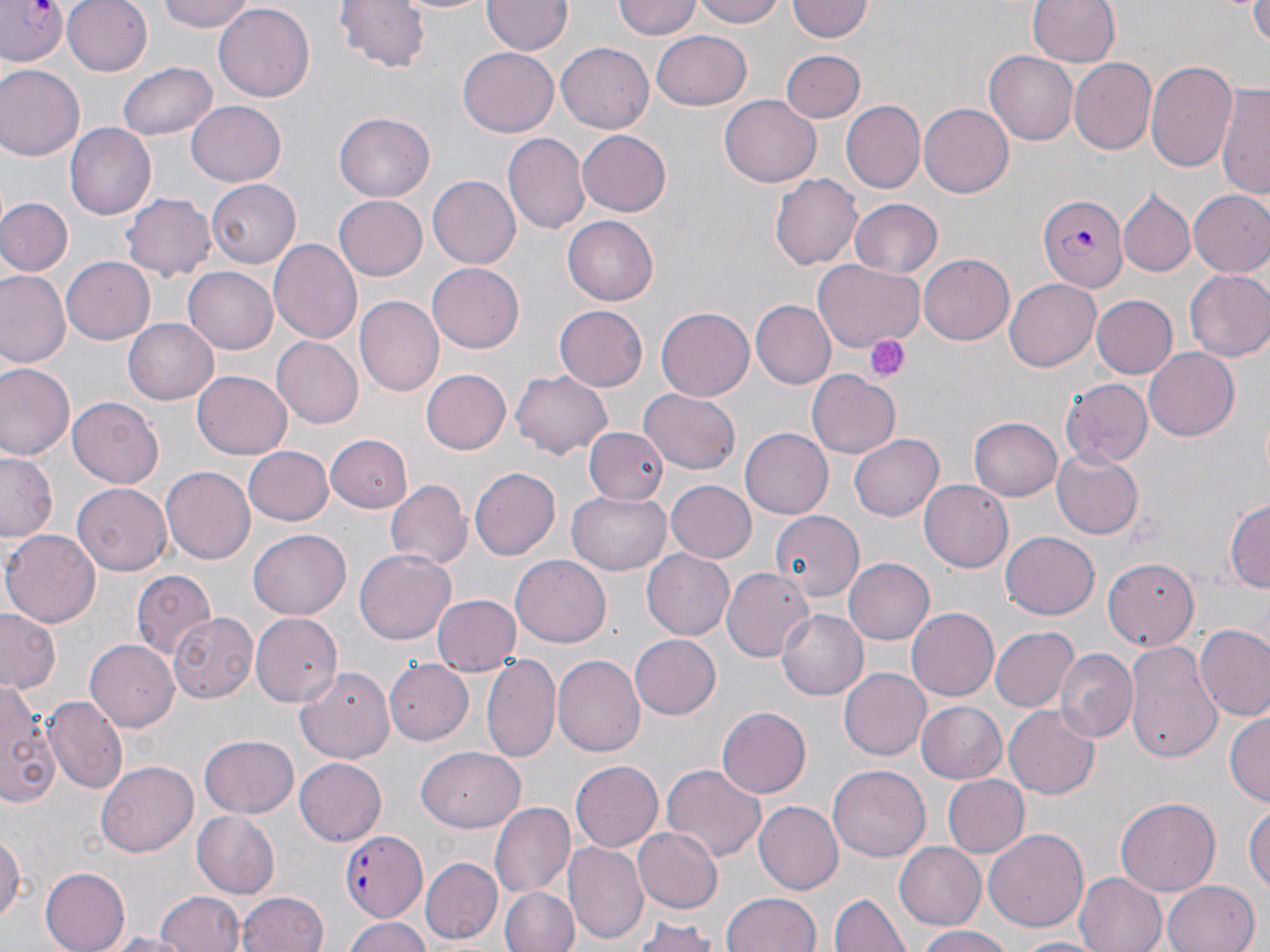

slide-level diagnosis = Plasmodium falciparum
uninfected red blood cell locations = approximate bounding boxes as (x1, y1, x2, y2) in pixels: (61, 0, 151, 75), (159, 0, 255, 31), (335, 0, 432, 73), (387, 0, 496, 15), (483, 0, 570, 56), (614, 0, 701, 41), (691, 0, 791, 27), (1026, 0, 1119, 70), (1250, 0, 1270, 45), (787, 1, 873, 43), (215, 4, 313, 100), (651, 30, 752, 111), (557, 41, 659, 132), (455, 47, 559, 137), (781, 49, 863, 122), (985, 52, 1080, 145), (1074, 60, 1158, 153), (1148, 60, 1239, 175), (119, 62, 216, 142), (0, 65, 85, 161), (1216, 83, 1270, 197), (719, 93, 820, 184), (842, 99, 924, 194), (188, 103, 285, 185), (918, 103, 1014, 197), (333, 112, 435, 203), (66, 123, 156, 219), (577, 129, 672, 217), (502, 133, 590, 236), (771, 172, 862, 269), (427, 175, 520, 270), (206, 180, 302, 268), (1118, 188, 1194, 278), (1188, 190, 1270, 278), (122, 193, 215, 280), (334, 195, 427, 279), (0, 196, 73, 276), (849, 198, 944, 279), (562, 216, 658, 306), (268, 238, 365, 343), (916, 255, 1013, 345), (62, 258, 154, 343), (427, 261, 527, 353), (812, 261, 923, 349), (182, 267, 277, 354), (1184, 268, 1270, 364), (1, 270, 69, 368), (1004, 278, 1102, 372), (1091, 294, 1179, 379), (356, 296, 443, 396), (751, 300, 837, 388), (552, 305, 649, 392), (656, 306, 755, 400), (123, 319, 217, 404), (272, 335, 363, 427), (1143, 347, 1240, 440), (0, 360, 75, 461), (421, 369, 510, 455), (511, 369, 614, 460), (806, 370, 900, 458), (193, 371, 293, 457), (1061, 378, 1153, 465), (639, 389, 741, 475), (67, 398, 165, 488), (970, 416, 1061, 501), (584, 425, 671, 503), (740, 427, 832, 516), (326, 431, 411, 513), (851, 433, 944, 519), (242, 446, 334, 526), (0, 451, 60, 542), (1052, 451, 1143, 537), (162, 465, 258, 563), (470, 467, 561, 561), (386, 479, 470, 572), (664, 481, 755, 563), (920, 481, 1013, 571), (71, 484, 172, 577), (569, 491, 673, 576), (1225, 498, 1269, 595), (770, 511, 864, 603), (2, 530, 100, 627), (249, 530, 350, 620), (1001, 531, 1098, 620), (354, 549, 456, 645), (642, 549, 734, 640), (1104, 554, 1201, 650), (511, 556, 611, 646), (844, 558, 936, 646), (720, 567, 814, 659), (132, 569, 218, 660), (431, 593, 520, 677), (776, 607, 870, 699), (907, 607, 999, 701), (0, 609, 62, 695), (169, 610, 259, 702), (250, 613, 341, 708), (1194, 626, 1270, 721), (991, 627, 1079, 710), (628, 633, 721, 719), (1124, 638, 1225, 762), (86, 640, 179, 731), (1055, 647, 1137, 742), (483, 653, 563, 765), (553, 655, 645, 757), (382, 657, 476, 745), (295, 666, 396, 762), (837, 667, 930, 760), (0, 685, 58, 808), (45, 695, 129, 794), (915, 701, 1007, 782), (1004, 704, 1100, 799), (715, 708, 811, 799), (1225, 712, 1269, 809), (198, 735, 298, 817), (416, 747, 526, 832), (295, 759, 386, 846), (96, 761, 200, 857), (570, 762, 663, 850), (662, 763, 767, 862), (828, 766, 930, 862), (943, 775, 1029, 858), (1115, 798, 1221, 895), (1245, 800, 1269, 902), (754, 801, 843, 895), (489, 802, 574, 900), (192, 812, 280, 898), (0, 825, 24, 927), (570, 825, 712, 938), (632, 827, 722, 913), (984, 828, 1089, 931), (566, 842, 647, 944), (894, 842, 985, 930), (422, 857, 502, 943), (40, 866, 130, 951), (1074, 872, 1166, 952), (1162, 880, 1262, 952), (500, 885, 579, 952), (237, 890, 329, 952), (722, 891, 822, 952), (154, 892, 245, 952), (830, 892, 909, 951), (344, 916, 434, 952), (632, 916, 722, 952), (913, 925, 1014, 952), (105, 931, 192, 951), (1012, 935, 1106, 951)
platelet locations = approximate bounding boxes as (x1, y1, x2, y2) in pixels: (863, 334, 909, 383)
preparation = thin blood film
field of view = one of a larger specimen
stain = May-Grünwald-Giemsa
modality = light microscopy
magnification = 1000x
Plasmodium falciparum-infected red blood cell locations = approximate bounding boxes as (x1, y1, x2, y2) in pixels: (0, 0, 67, 66), (1039, 193, 1128, 294), (342, 830, 427, 918)
image size = 1270×952 pixels